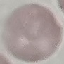
malaria status = uninfected
stain = Giemsa
preparation = thin blood film
image type = cell patch, automatically extracted from a larger field of view and resized to 64 × 64 pixels
capture = smartphone through the microscope eyepiece